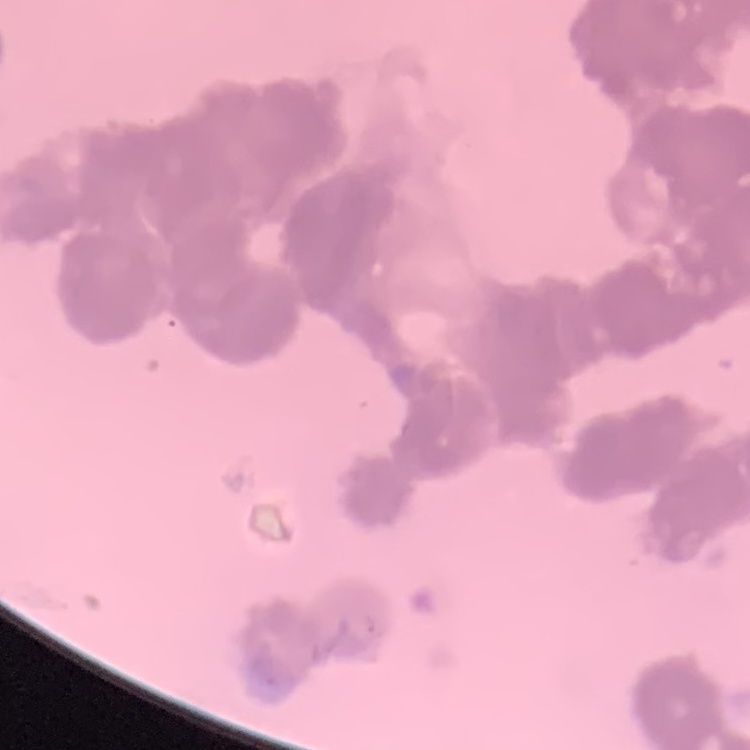 The erythrocytes show rouleaux formation. Square crop of a larger photomicrograph. Stained with either Field's or Giemsa. Thin blood film.